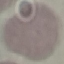 Result: no malaria parasites detected. Acquired by smartphone through the microscope eyepiece. Thin blood smear. Cell patch, automatically extracted from a larger field of view and resized to 64 × 64 pixels. Giemsa-stained preparation.